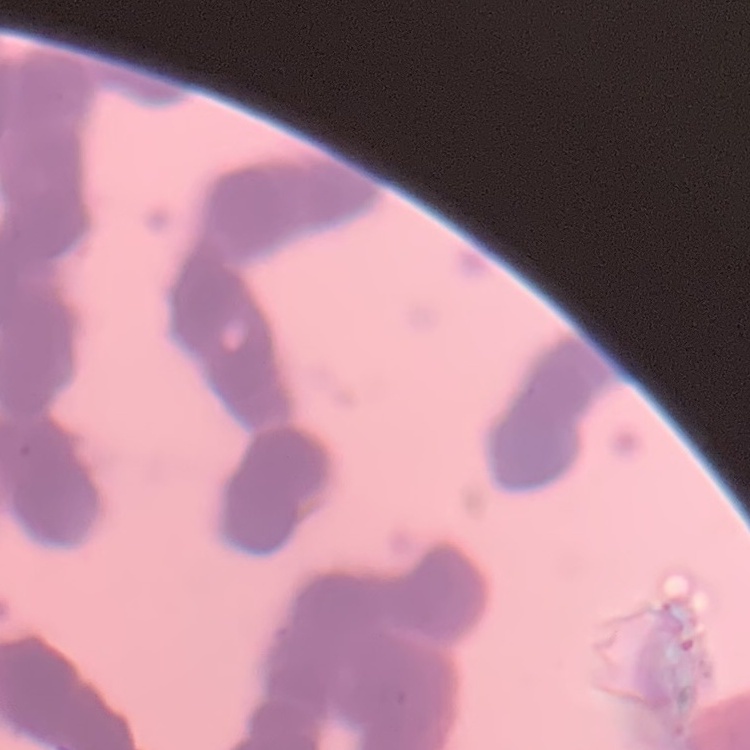
The erythrocytes exhibit rouleaux formation. Field's or Giemsa stain. Square crop of a larger photomicrograph. Thin blood film.